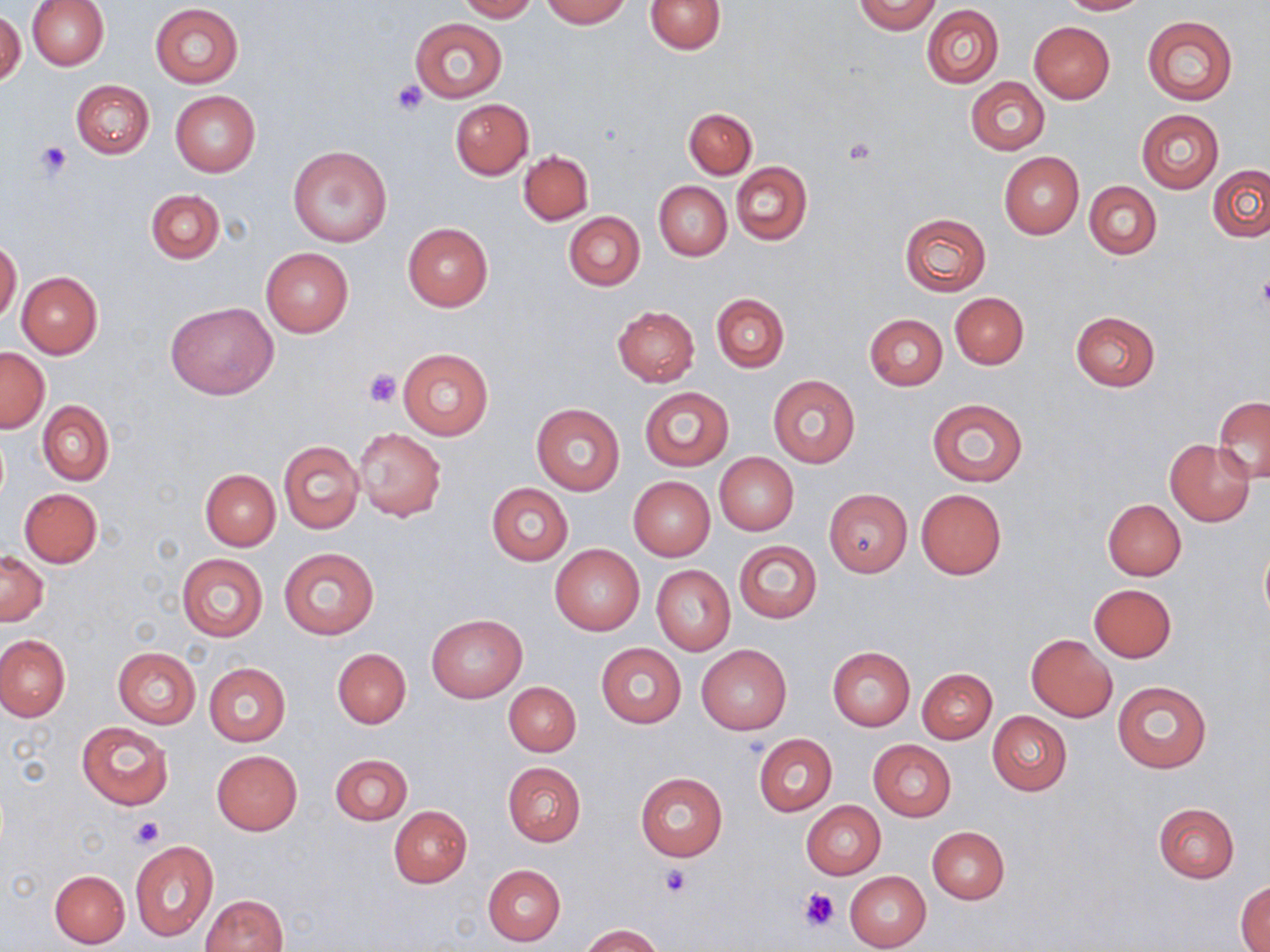

slide-level diagnosis = no evidence of blood parasites
preparation = thin blood film
modality = light microscopy
platelet locations = approximate bounding boxes as [x1, y1, x2, y2] in pixels: [390, 79, 428, 115], [846, 138, 877, 164], [36, 141, 71, 178], [1256, 276, 1270, 316], [364, 368, 402, 409], [129, 815, 164, 850], [660, 866, 693, 898], [802, 888, 840, 932]
image size = 1270×952 pixels
magnification = 1000x
field of view = single
uninfected red blood cell locations = approximate bounding boxes as [x1, y1, x2, y2] in pixels: [27, 0, 108, 70], [455, 0, 538, 22], [541, 0, 630, 27], [645, 0, 726, 54], [1057, 0, 1148, 15], [854, 1, 942, 34], [150, 3, 243, 87], [922, 4, 1004, 88], [1, 10, 26, 86], [1142, 16, 1238, 104], [409, 19, 507, 102], [1029, 21, 1115, 103], [965, 77, 1049, 155], [71, 80, 154, 159], [170, 90, 260, 176], [450, 98, 534, 179], [684, 107, 756, 179], [1135, 108, 1224, 193], [288, 143, 393, 248], [519, 150, 593, 225], [999, 152, 1084, 238], [731, 162, 812, 245], [1208, 163, 1270, 242], [654, 182, 731, 260], [1084, 182, 1161, 259], [146, 189, 224, 264], [564, 212, 644, 291], [899, 212, 991, 296], [403, 223, 493, 310], [0, 240, 21, 324], [261, 248, 353, 337], [17, 271, 103, 358], [711, 292, 789, 373], [950, 292, 1028, 369], [166, 301, 278, 399], [612, 305, 699, 386], [1070, 311, 1160, 391], [864, 313, 947, 389], [0, 347, 49, 432], [398, 347, 493, 440], [767, 375, 860, 468], [640, 387, 732, 470], [1212, 397, 1270, 483], [927, 398, 1027, 485], [37, 400, 113, 485], [531, 401, 625, 496], [354, 427, 447, 520], [278, 439, 364, 534], [1164, 439, 1255, 526], [715, 453, 798, 535], [200, 469, 280, 549], [628, 476, 715, 561], [487, 483, 572, 565], [19, 488, 102, 568], [916, 488, 1006, 579], [824, 489, 912, 577], [1103, 499, 1186, 579], [734, 541, 822, 623], [1259, 542, 1270, 630], [550, 545, 645, 636], [278, 547, 378, 639], [0, 552, 48, 626], [176, 553, 268, 643], [652, 566, 735, 654], [1088, 584, 1176, 662], [426, 614, 526, 703], [0, 634, 71, 722], [1026, 634, 1117, 721], [595, 643, 686, 728], [697, 645, 791, 735], [112, 647, 201, 728], [827, 647, 914, 731], [332, 648, 411, 727], [205, 663, 290, 746], [917, 667, 996, 743], [1112, 680, 1211, 772], [504, 682, 580, 756], [987, 710, 1072, 795], [76, 720, 173, 810], [753, 734, 836, 815], [868, 740, 956, 822], [212, 750, 301, 835], [330, 754, 412, 825], [502, 761, 586, 846], [634, 772, 728, 861], [802, 801, 886, 879], [1152, 802, 1239, 883], [389, 806, 472, 887], [926, 825, 1010, 903], [130, 840, 217, 940], [482, 864, 566, 946], [49, 870, 130, 949], [845, 871, 932, 951], [1235, 881, 1270, 950], [201, 894, 287, 952], [581, 924, 662, 952]
stain = May-Grünwald-Giemsa